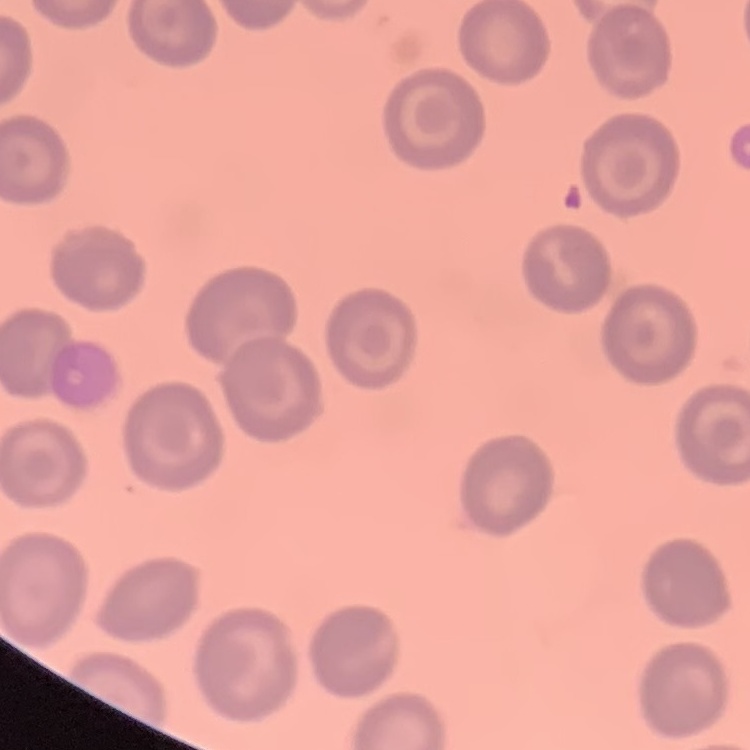
The erythrocytes exhibit no rouleaux formation. Square crop of a larger photomicrograph. Thin peripheral smear. Stained with either Field's or Giemsa.